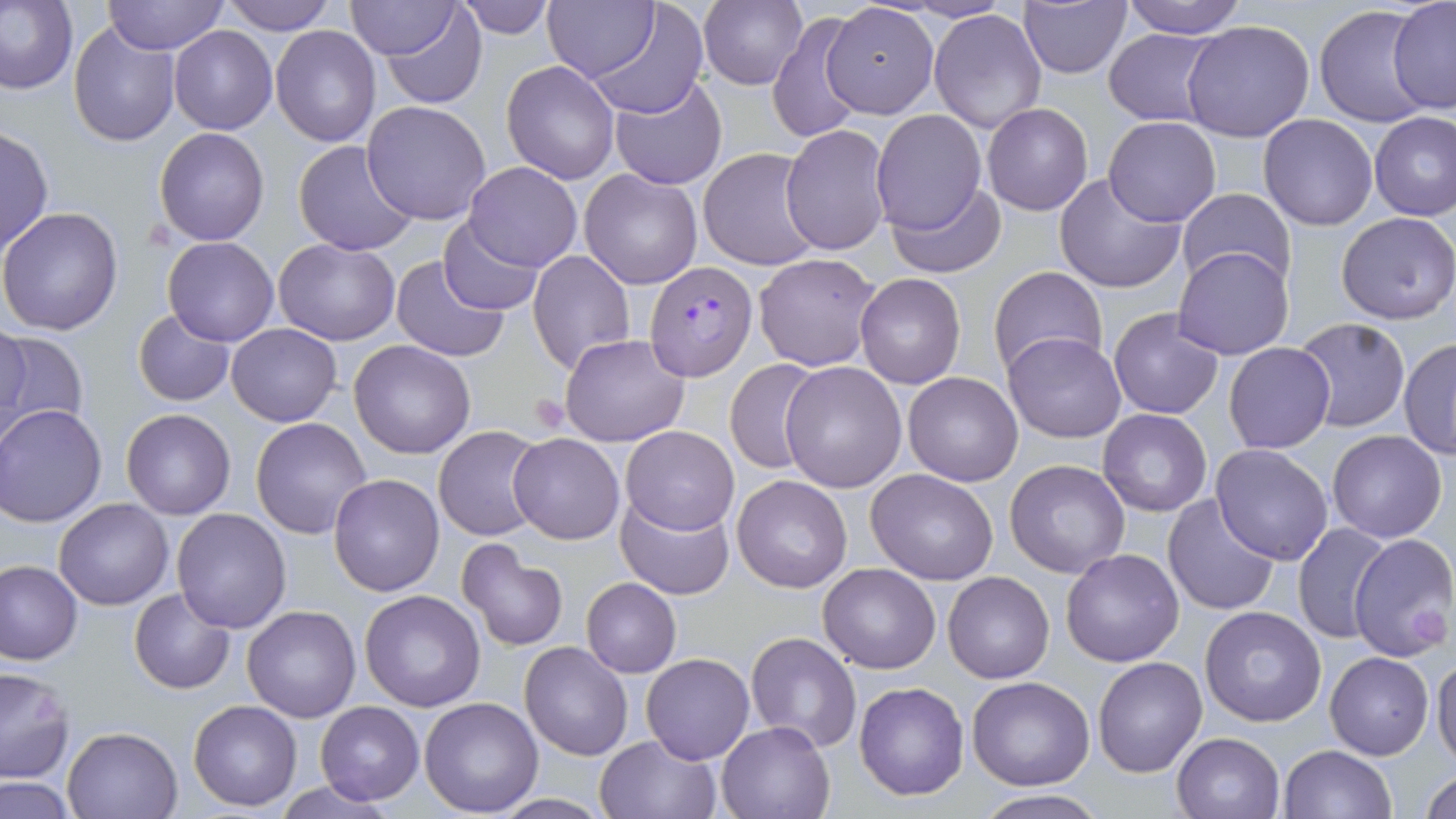
Approximate bounding boxes as named x1/y1/x2/y2 corners in pixels. Uninfected red blood cell locations: (x1=0, y1=0, x2=78, y2=95), (x1=103, y1=0, x2=229, y2=54), (x1=220, y1=0, x2=336, y2=36), (x1=699, y1=0, x2=809, y2=91), (x1=1122, y1=0, x2=1247, y2=39), (x1=1387, y1=0, x2=1456, y2=114), (x1=341, y1=1, x2=466, y2=61), (x1=378, y1=1, x2=488, y2=109), (x1=453, y1=1, x2=555, y2=38), (x1=543, y1=1, x2=658, y2=82), (x1=589, y1=2, x2=709, y2=118), (x1=1018, y1=2, x2=1134, y2=78), (x1=821, y1=3, x2=939, y2=120), (x1=1313, y1=5, x2=1439, y2=128), (x1=929, y1=8, x2=1047, y2=134), (x1=768, y1=13, x2=868, y2=145), (x1=1181, y1=20, x2=1315, y2=142), (x1=69, y1=22, x2=180, y2=149), (x1=270, y1=24, x2=380, y2=147), (x1=168, y1=25, x2=277, y2=134), (x1=1104, y1=28, x2=1225, y2=126), (x1=500, y1=59, x2=621, y2=184), (x1=608, y1=75, x2=728, y2=188), (x1=361, y1=101, x2=494, y2=224), (x1=981, y1=102, x2=1093, y2=215), (x1=870, y1=111, x2=989, y2=235), (x1=1368, y1=111, x2=1456, y2=221), (x1=1258, y1=114, x2=1378, y2=230), (x1=1102, y1=116, x2=1222, y2=226), (x1=782, y1=123, x2=891, y2=256), (x1=0, y1=125, x2=54, y2=257), (x1=154, y1=126, x2=269, y2=246), (x1=294, y1=140, x2=420, y2=256), (x1=699, y1=147, x2=822, y2=272), (x1=464, y1=162, x2=581, y2=272), (x1=579, y1=167, x2=702, y2=290), (x1=1054, y1=173, x2=1186, y2=295), (x1=891, y1=184, x2=1006, y2=276), (x1=1175, y1=188, x2=1298, y2=295), (x1=0, y1=207, x2=123, y2=336), (x1=1336, y1=211, x2=1456, y2=325), (x1=437, y1=217, x2=544, y2=313), (x1=163, y1=237, x2=278, y2=347), (x1=273, y1=237, x2=400, y2=346), (x1=1173, y1=246, x2=1295, y2=360), (x1=529, y1=249, x2=636, y2=376), (x1=753, y1=252, x2=883, y2=372), (x1=390, y1=254, x2=509, y2=362), (x1=989, y1=266, x2=1109, y2=380), (x1=855, y1=275, x2=967, y2=390), (x1=1108, y1=307, x2=1226, y2=420), (x1=134, y1=310, x2=236, y2=406), (x1=1292, y1=316, x2=1411, y2=432), (x1=0, y1=319, x2=30, y2=444), (x1=227, y1=323, x2=342, y2=426), (x1=0, y1=329, x2=91, y2=442), (x1=559, y1=332, x2=691, y2=446), (x1=1003, y1=332, x2=1127, y2=442), (x1=1398, y1=338, x2=1456, y2=460), (x1=348, y1=341, x2=474, y2=459), (x1=1223, y1=341, x2=1337, y2=453), (x1=724, y1=359, x2=823, y2=474), (x1=780, y1=361, x2=907, y2=492), (x1=903, y1=371, x2=1023, y2=487), (x1=0, y1=404, x2=107, y2=528), (x1=120, y1=408, x2=236, y2=519), (x1=1097, y1=408, x2=1213, y2=517), (x1=251, y1=417, x2=374, y2=540), (x1=622, y1=425, x2=740, y2=535), (x1=434, y1=426, x2=545, y2=541), (x1=1328, y1=429, x2=1447, y2=543), (x1=508, y1=432, x2=625, y2=544), (x1=1210, y1=443, x2=1335, y2=565), (x1=1004, y1=459, x2=1130, y2=579), (x1=866, y1=469, x2=1000, y2=585), (x1=329, y1=474, x2=445, y2=595), (x1=732, y1=475, x2=853, y2=592), (x1=616, y1=492, x2=735, y2=601), (x1=1162, y1=493, x2=1281, y2=615), (x1=53, y1=497, x2=174, y2=611), (x1=171, y1=507, x2=292, y2=631), (x1=1292, y1=522, x2=1396, y2=645), (x1=1348, y1=531, x2=1455, y2=662), (x1=456, y1=541, x2=569, y2=651), (x1=1060, y1=548, x2=1186, y2=666), (x1=0, y1=561, x2=83, y2=664), (x1=818, y1=563, x2=941, y2=674), (x1=942, y1=571, x2=1054, y2=683), (x1=582, y1=577, x2=681, y2=678), (x1=129, y1=587, x2=235, y2=694), (x1=358, y1=590, x2=486, y2=712), (x1=242, y1=604, x2=362, y2=722), (x1=1201, y1=606, x2=1327, y2=728), (x1=745, y1=632, x2=862, y2=753), (x1=519, y1=640, x2=634, y2=760), (x1=1325, y1=649, x2=1434, y2=759), (x1=641, y1=652, x2=754, y2=764), (x1=1092, y1=656, x2=1207, y2=778), (x1=1431, y1=658, x2=1456, y2=768), (x1=0, y1=667, x2=75, y2=783), (x1=966, y1=676, x2=1095, y2=789), (x1=854, y1=680, x2=970, y2=801), (x1=0, y1=690, x2=127, y2=808), (x1=419, y1=696, x2=543, y2=816), (x1=189, y1=699, x2=303, y2=811), (x1=316, y1=700, x2=424, y2=803), (x1=716, y1=719, x2=838, y2=818), (x1=62, y1=725, x2=184, y2=817), (x1=1171, y1=731, x2=1285, y2=819), (x1=593, y1=733, x2=722, y2=819), (x1=1279, y1=745, x2=1395, y2=819), (x1=1422, y1=769, x2=1456, y2=819), (x1=0, y1=777, x2=77, y2=819), (x1=275, y1=779, x2=395, y2=817), (x1=972, y1=791, x2=1111, y2=818), (x1=489, y1=794, x2=611, y2=818). Plasmodium falciparum-infected red blood cell locations: (x1=644, y1=261, x2=757, y2=381). Platelet locations: (x1=530, y1=394, x2=572, y2=433). Slide-level diagnosis: Plasmodium falciparum. May-Grünwald-Giemsa-stained preparation. Image is 1456×819 pixels. Single field of view. Captured at 1000x magnification. Light microscopy. Thin blood film.